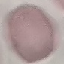

malaria_status: uninfected
capture: smartphone camera at the microscope eyepiece
stain: Giemsa
preparation: thin smear
image_type: cell patch, automatically extracted from a larger field of view and resized to 64 × 64 pixels